Comment on the morphology of the erythrocytes.
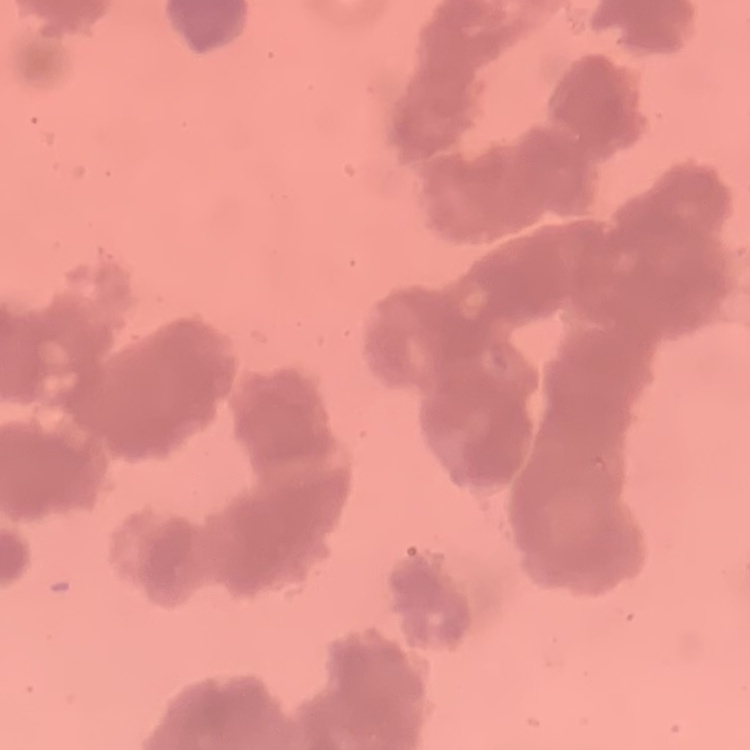

They show rouleaux formation.

Summary:
  - Preparation: thin blood film
  - Stain: Field's or Giemsa
  - Image type: square crop of a larger photomicrograph